Point out each Plasmodium parasite.
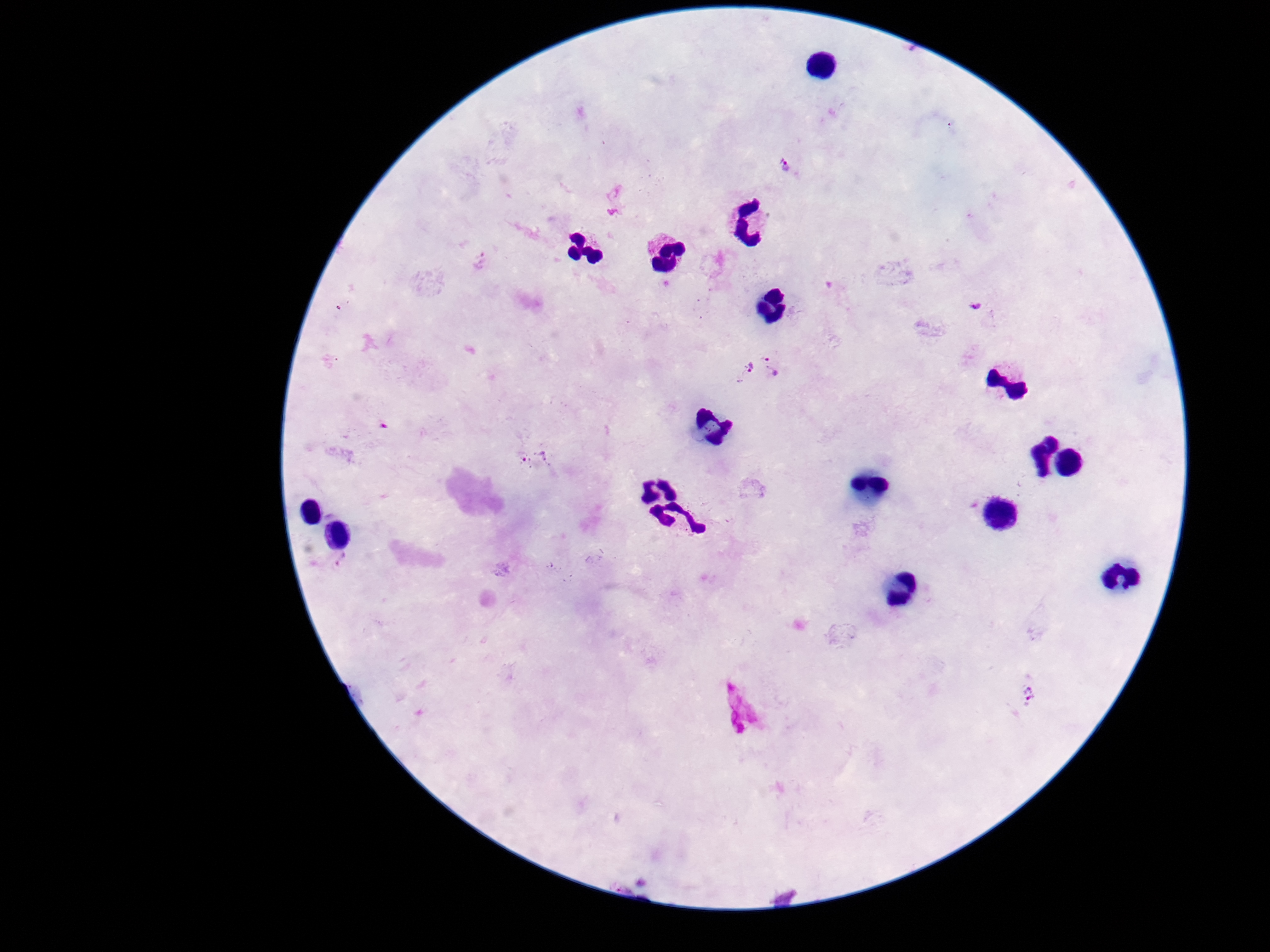

Approximate object centers, in pixels from the top-left corner.
Plasmodium parasites: (x=785, y=165), (x=480, y=259), (x=978, y=305), (x=774, y=365), (x=741, y=372), (x=539, y=460), (x=345, y=564), (x=1029, y=695).

image size = 1270×952 pixels
patient malaria status = infected
magnification = 100x
field of view = single
preparation = thick peripheral-blood smear
stain = Giemsa
capture = smartphone camera through the microscope eyepiece